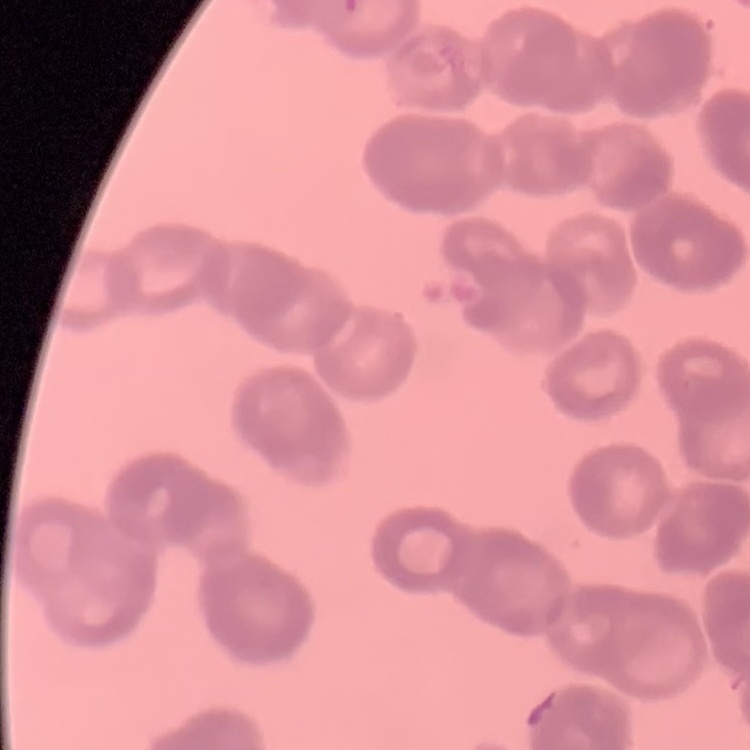
The erythrocytes exhibit rouleaux formation. Square crop of a larger photomicrograph. Field's or Giemsa stain. Thin peripheral smear.